Locate and identify every blood parasite.
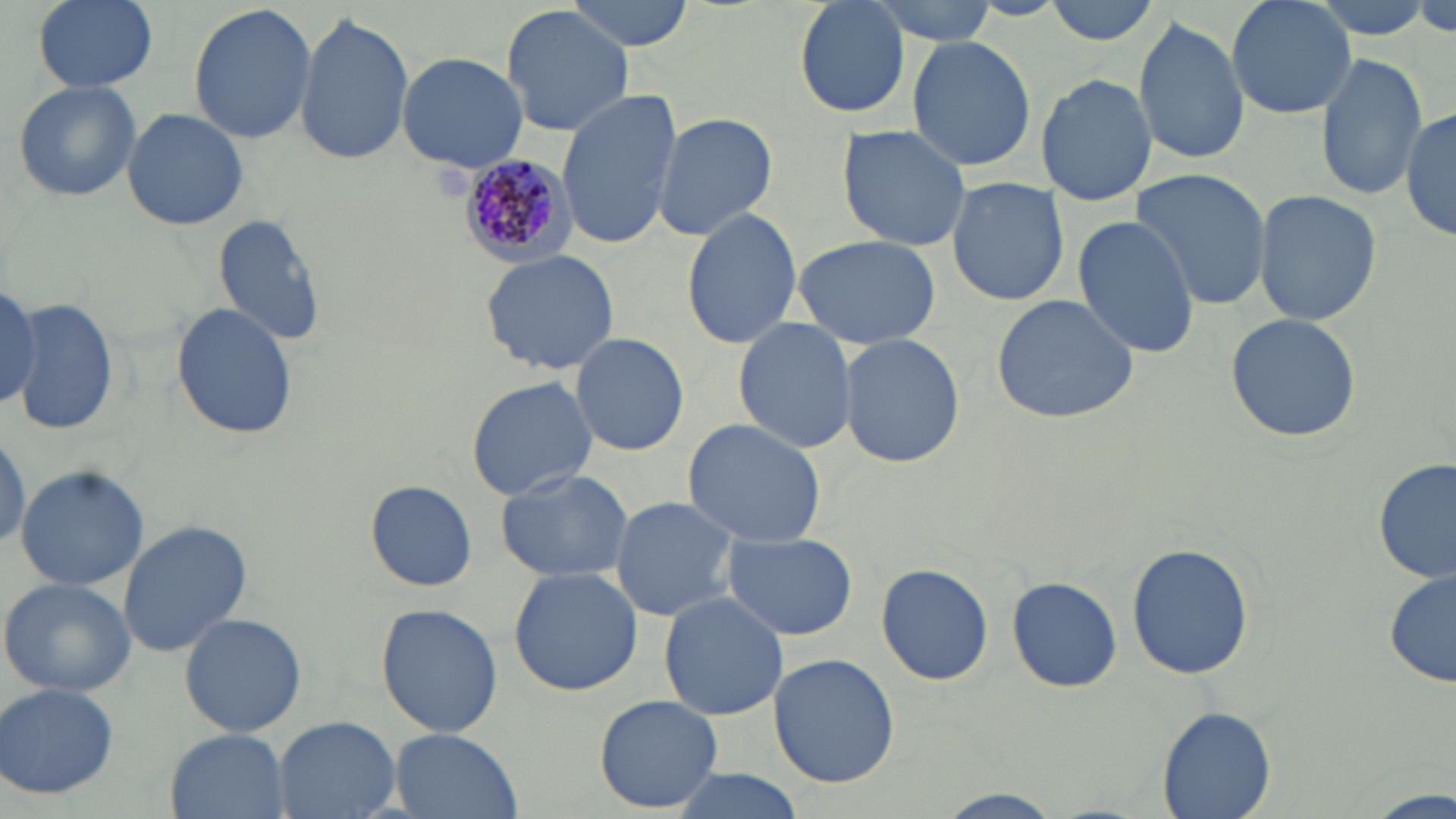
Approximate bounding boxes as [x1, y1, x2, y2] in pixels.
Plasmodium malariae-infected red blood cells: [452, 157, 578, 267].
No Plasmodium falciparum, Plasmodium ovale, Plasmodium vivax, Babesia divergens, or Trypanosoma brucei observed.

slide-level diagnosis = Plasmodium malariae
modality = optical microscopy
stain = May-Grünwald-Giemsa
uninfected red blood cell locations = approximate bounding boxes as [x1, y1, x2, y2] in pixels: [33, 0, 158, 92], [567, 0, 697, 49], [792, 0, 910, 118], [862, 0, 1006, 43], [1044, 0, 1165, 46], [1224, 0, 1357, 120], [187, 3, 317, 146], [501, 5, 635, 137], [294, 12, 414, 165], [1133, 17, 1249, 166], [908, 34, 1036, 175], [1314, 50, 1428, 203], [395, 51, 529, 171], [1039, 72, 1158, 205], [12, 81, 143, 204], [556, 90, 683, 251], [1403, 102, 1456, 244], [121, 107, 249, 231], [653, 111, 778, 242], [837, 125, 971, 252], [1128, 168, 1272, 311], [946, 175, 1070, 307], [1253, 190, 1382, 326], [682, 205, 803, 347], [211, 212, 329, 347], [1072, 216, 1203, 359], [791, 233, 943, 350], [482, 248, 621, 375], [0, 285, 42, 409], [991, 293, 1140, 425], [14, 297, 119, 436], [170, 303, 298, 438], [1225, 312, 1363, 443], [734, 315, 857, 455], [569, 333, 691, 457], [837, 333, 964, 468], [464, 374, 597, 500], [682, 419, 827, 548], [1375, 459, 1455, 586], [16, 464, 149, 592], [493, 467, 635, 582], [365, 479, 477, 592], [608, 495, 747, 622], [116, 520, 252, 658], [723, 533, 857, 640], [1127, 541, 1253, 681], [874, 561, 994, 687], [508, 566, 644, 697], [1383, 568, 1456, 690], [1007, 576, 1123, 693], [0, 577, 136, 696], [658, 592, 789, 720], [376, 603, 503, 738], [179, 612, 308, 737], [767, 652, 900, 788], [1, 682, 121, 800], [592, 695, 725, 813], [1156, 706, 1276, 819], [273, 715, 400, 819], [165, 728, 290, 819], [388, 728, 523, 819], [664, 770, 809, 819], [926, 789, 1071, 817], [1364, 790, 1450, 818]
preparation = thin blood smear
field of view = single
magnification = 1000x
image size = 1456×819 pixels